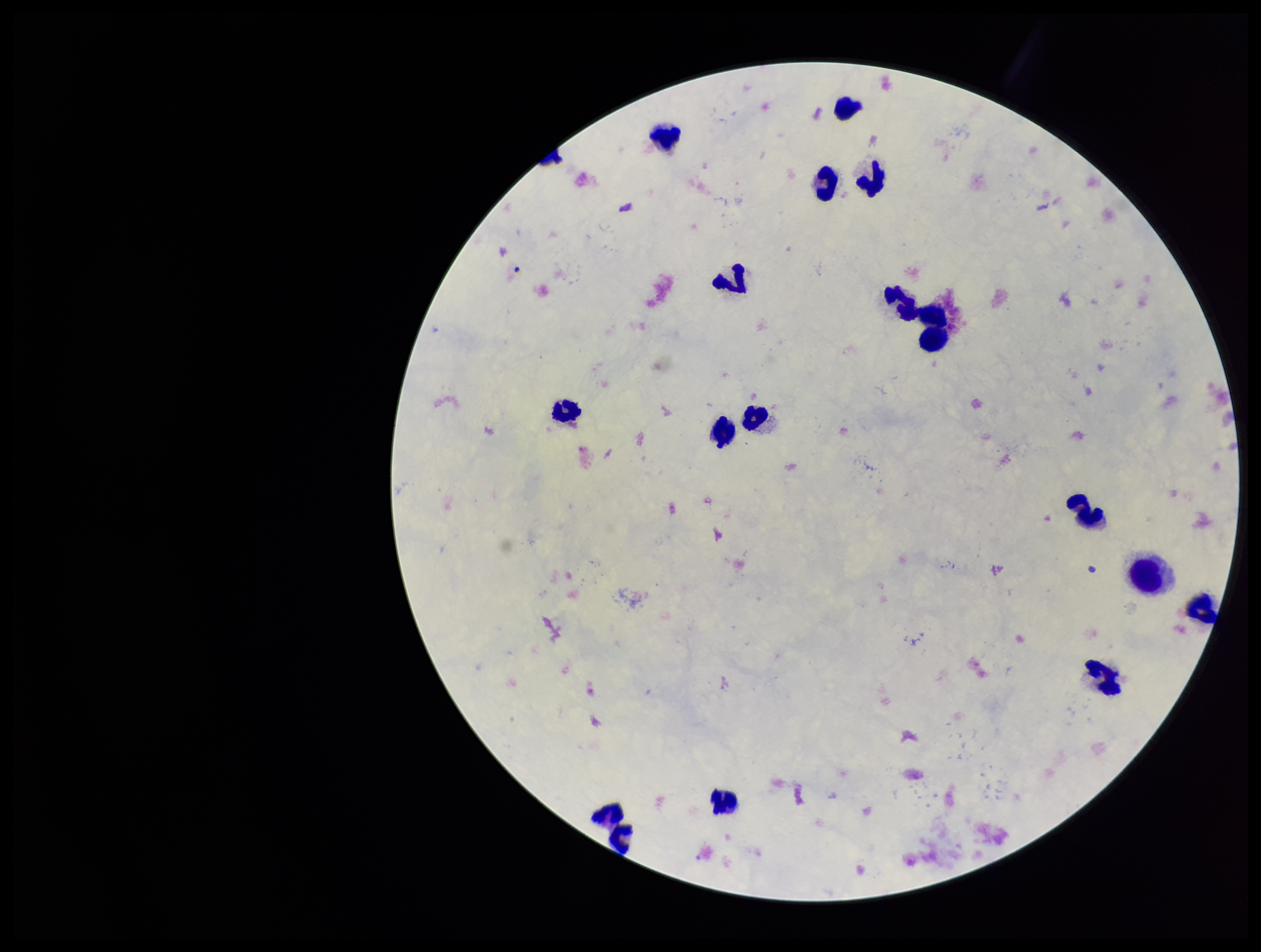
field of view = single
image size = 1261×952 pixels
stain = Giemsa
leukocyte count = 16
parasite count = 0
preparation = thick smear
Plasmodium parasites = none seen
capture = smartphone photograph through the microscope eyepiece
patient malaria status = negative